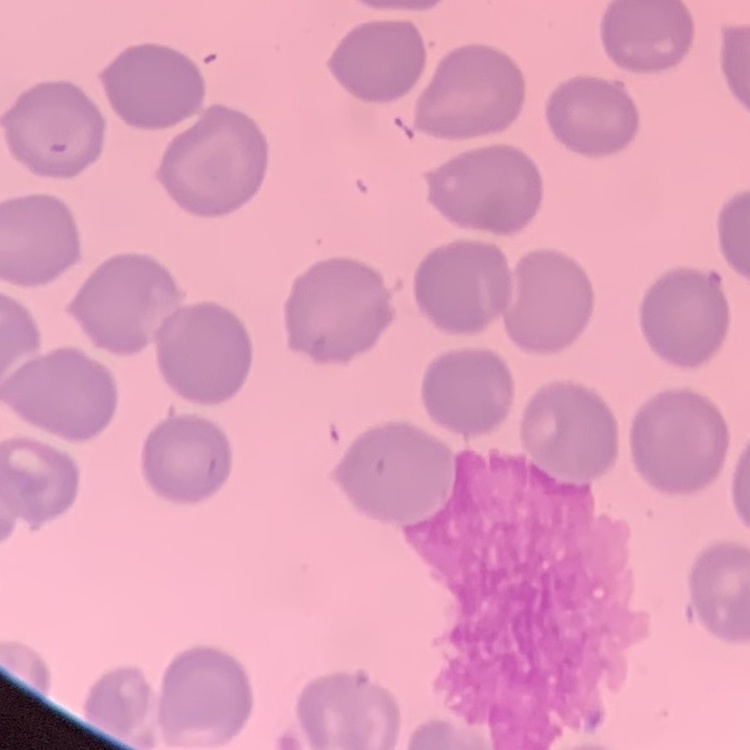

The erythrocytes show no rouleaux formation. One tile cut from a larger photomicrograph. Field's or Giemsa stain. Thin peripheral smear.